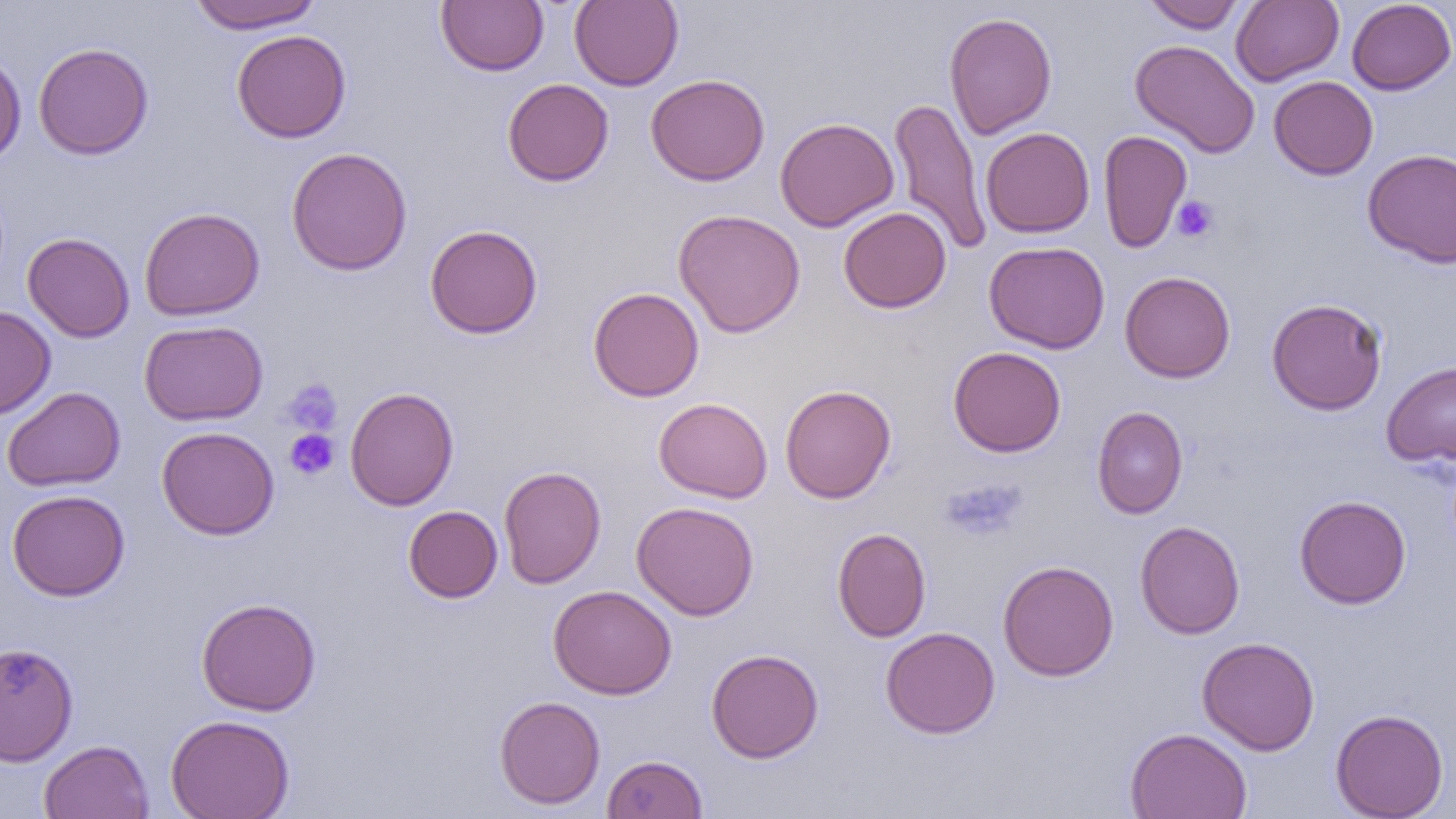 Approximate bounding boxes as (x1,y1)-(x2,y2) corner pairs in pixels. Platelet locations: (1172,196)-(1219,243), (283,379)-(343,436), (284,429)-(339,480), (940,478)-(1026,542). Uninfected red blood cell locations: (185,0)-(325,32), (436,0)-(549,76), (569,0)-(684,91), (1143,0)-(1247,33), (1231,0)-(1344,86), (1346,0)-(1456,95), (943,11)-(1057,139), (231,29)-(352,143), (1130,39)-(1260,158), (33,42)-(153,159), (0,49)-(27,167), (645,73)-(770,186), (1268,76)-(1378,180), (503,78)-(614,186), (889,97)-(991,256), (775,116)-(899,232), (980,127)-(1095,238), (1098,129)-(1192,254), (286,147)-(413,276), (1362,148)-(1456,267), (139,206)-(265,321), (839,207)-(951,313), (672,208)-(806,338), (424,224)-(543,339), (22,232)-(135,343), (984,241)-(1110,354), (1119,270)-(1236,383), (588,287)-(704,402), (1266,297)-(1388,415), (0,306)-(56,419), (139,320)-(268,426), (948,346)-(1067,457), (1381,360)-(1456,467), (780,384)-(896,504), (2,386)-(125,491), (345,387)-(459,511), (653,397)-(773,503), (1092,406)-(1188,519), (157,426)-(280,540), (498,466)-(606,588), (6,489)-(130,601), (1295,495)-(1411,609), (631,501)-(760,621), (403,505)-(503,603), (1134,520)-(1246,639), (831,527)-(932,642), (997,559)-(1119,681), (548,584)-(677,699), (196,597)-(322,716), (880,626)-(1000,738), (1197,636)-(1320,756), (0,643)-(78,765), (705,648)-(824,763), (494,695)-(606,809), (1330,708)-(1449,818), (166,714)-(295,819), (1125,727)-(1252,819), (39,739)-(154,819), (601,753)-(708,818). Slide-level diagnosis: no evidence of blood parasites. One field of a larger specimen. Image is 1456×819 pixels. Optical microscopy. Thin blood smear. 1000x magnification.